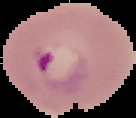

Summary:
  - Result: Plasmodium parasites identified
  - Image type: cell region segmented out of the field of view; surrounding area masked to black
  - Image size: 136×118 pixels
  - Preparation: thin blood film